Classify this cell by malaria status.
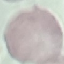
It is uninfected.

capture: smartphone through the microscope eyepiece
preparation: thin blood smear
stain: Giemsa
image_type: cell patch, automatically extracted from a larger field of view and resized to 64 × 64 pixels